Describe the morphology of the erythrocytes.
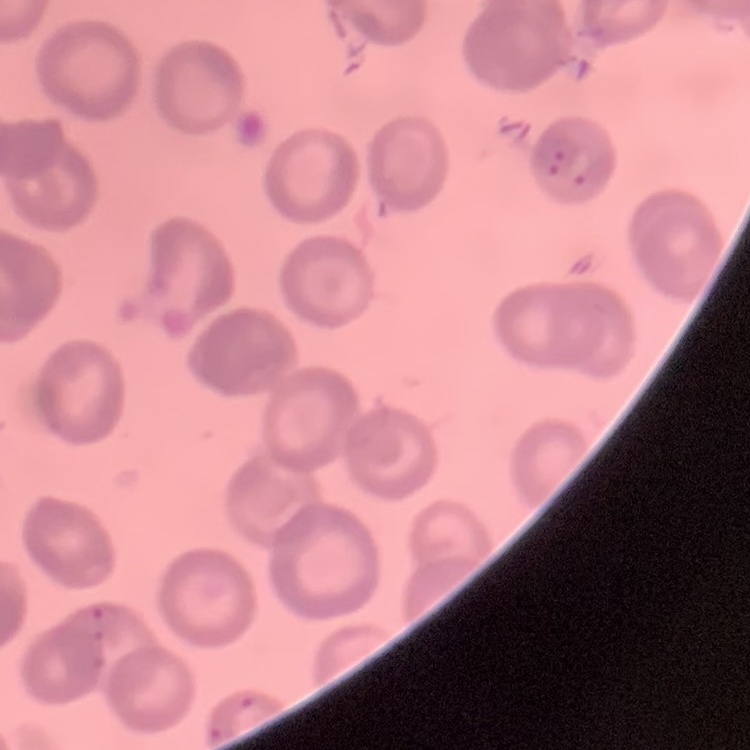
They show no rouleaux formation.

Summary:
  - Stain: Field's or Giemsa
  - Image type: square crop of a larger photomicrograph
  - Preparation: thin blood film